Identify the blood parasite species.
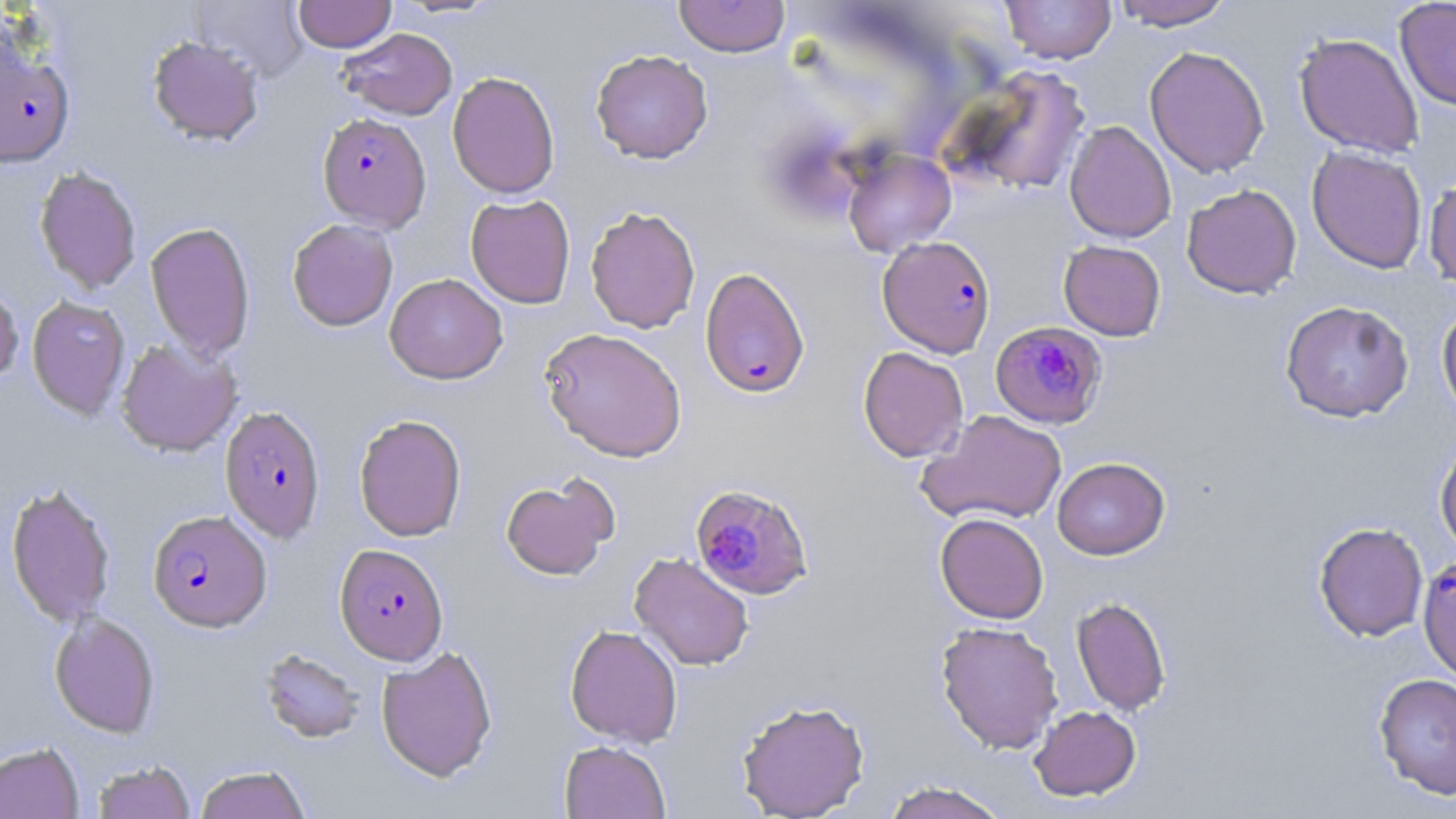
Plasmodium falciparum.

Summary:
  - Coordinate format: approximate bounding boxes as [x1, y1, x2, y2] in pixels
  - Uninfected red blood cell locations: [190, 0, 310, 83], [293, 0, 396, 51], [392, 0, 502, 18], [673, 0, 790, 57], [999, 0, 1116, 64], [1111, 0, 1235, 30], [1395, 0, 1456, 110], [337, 28, 457, 120], [1294, 32, 1424, 159], [148, 36, 264, 146], [1144, 45, 1270, 179], [590, 49, 713, 163], [948, 65, 1092, 197], [447, 71, 560, 199], [1064, 120, 1176, 243], [1306, 146, 1427, 273], [842, 149, 956, 257], [34, 166, 142, 294], [1423, 170, 1456, 293], [1181, 184, 1302, 299], [465, 194, 576, 308], [585, 205, 701, 334], [287, 218, 398, 331], [145, 221, 256, 360], [1059, 240, 1166, 341], [384, 273, 508, 384], [0, 281, 23, 386], [26, 295, 130, 419], [1280, 300, 1414, 423], [1437, 303, 1456, 427], [539, 327, 687, 463], [115, 338, 242, 457], [858, 346, 969, 462], [919, 410, 1067, 526], [353, 413, 467, 541], [1434, 437, 1456, 558], [1052, 457, 1170, 560], [500, 474, 617, 581], [5, 480, 116, 627], [935, 513, 1049, 624], [1314, 521, 1429, 641], [629, 552, 754, 671], [1071, 596, 1171, 717], [49, 611, 160, 737], [935, 620, 1063, 754], [565, 624, 683, 747], [376, 645, 497, 782], [259, 648, 366, 744], [1373, 673, 1456, 800], [735, 698, 870, 818], [1029, 705, 1141, 801], [559, 739, 670, 819], [0, 742, 84, 819], [92, 760, 195, 819], [194, 765, 311, 818], [880, 780, 1011, 819]
  - Plasmodium falciparum-infected red blood cell locations: [0, 43, 74, 166], [317, 112, 431, 232], [878, 235, 996, 357], [699, 267, 810, 399], [989, 324, 1113, 432], [219, 405, 327, 543], [689, 482, 814, 601], [147, 509, 271, 631], [335, 543, 448, 665], [1417, 556, 1456, 681]
  - Stain: May-Grünwald-Giemsa
  - Preparation: thin blood smear
  - Magnification: 1000x
  - Image size: 1456×819 pixels
  - Field of view: single
  - Modality: light microscopy